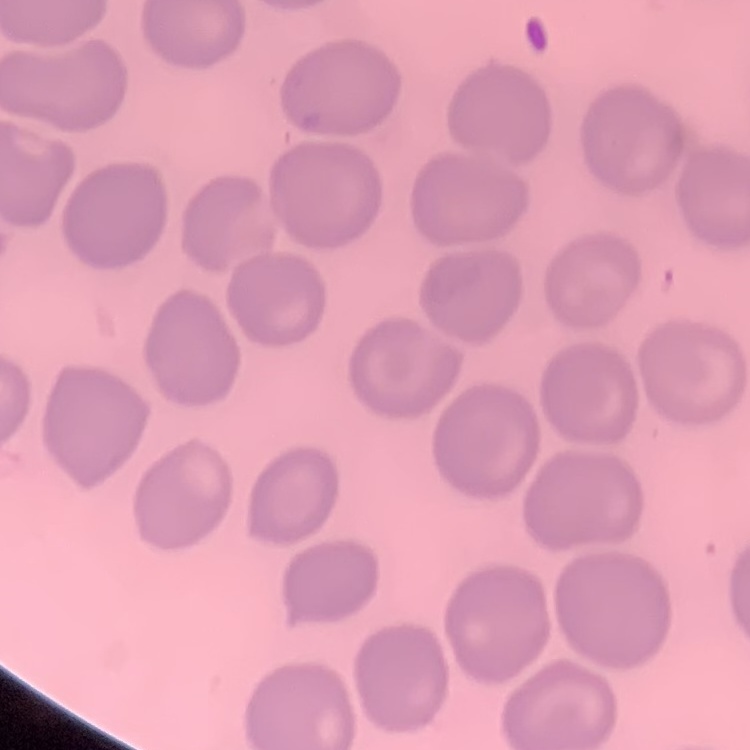

Summary:
  - Erythrocyte morphology: no rouleaux formation
  - Preparation: thin blood smear
  - Stain: Field's or Giemsa
  - Image type: one tile cut from a larger photomicrograph